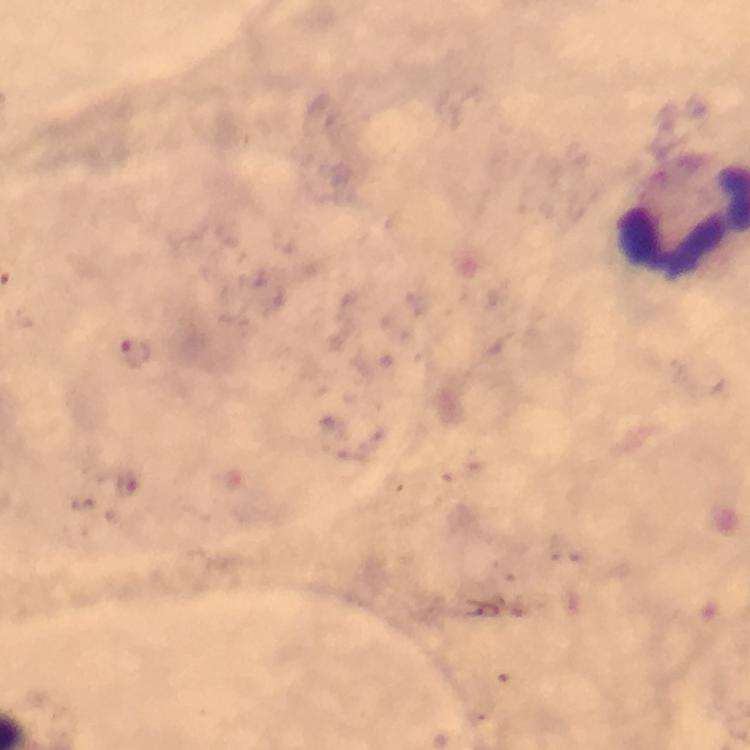
{
  "immersion_oil": "applied",
  "stain": "Giemsa",
  "cropped_from": "one field of view",
  "plasmodium_parasite_locations": "approximate centers as (x, y) in pixels: (134, 354), (128, 485)",
  "context": "from a malaria diagnostic workup",
  "capture": "smartphone mounted on the microscope",
  "magnification": "100x",
  "preparation": "thick smear",
  "image_size": "750×750 pixels"
}